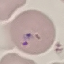

Result: malaria parasites detected. Acquired by smartphone through the microscope eyepiece. Cell patch, automatically extracted from a larger field of view and resized to 64 × 64 pixels. Giemsa stain. Thin blood film.